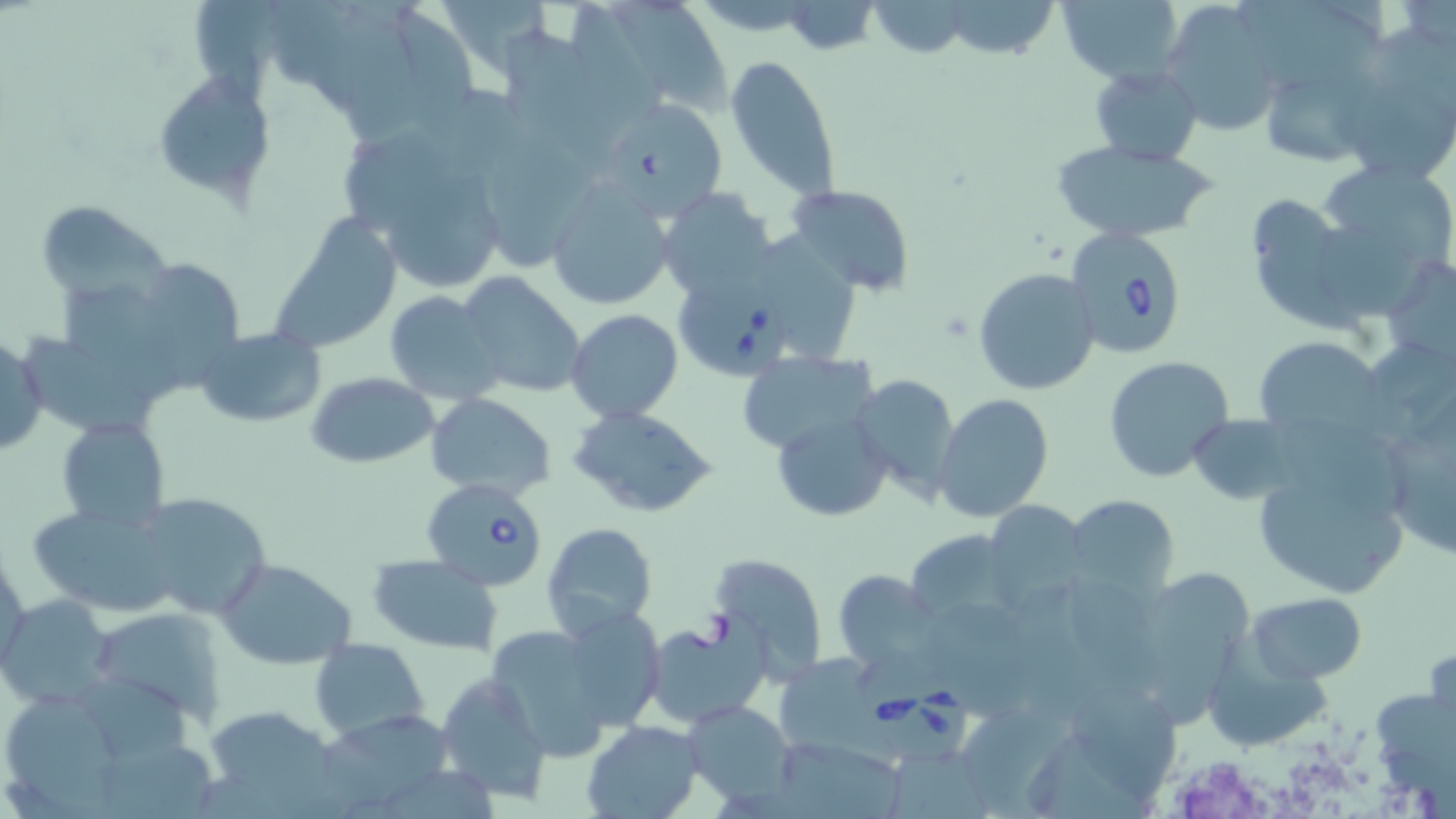
Summary:
  - Coordinate format: approximate bounding boxes as named x1/y1/x2/y2 corners in pixels
  - Uninfected red blood cell locations: (x1=937, y1=0, x2=1063, y2=60), (x1=1055, y1=0, x2=1182, y2=85), (x1=1241, y1=0, x2=1383, y2=78), (x1=193, y1=1, x2=289, y2=114), (x1=615, y1=1, x2=738, y2=112), (x1=868, y1=2, x2=974, y2=58), (x1=1157, y1=2, x2=1285, y2=134), (x1=387, y1=3, x2=476, y2=139), (x1=337, y1=12, x2=420, y2=147), (x1=502, y1=29, x2=623, y2=163), (x1=725, y1=55, x2=841, y2=200), (x1=1089, y1=65, x2=1205, y2=166), (x1=150, y1=70, x2=274, y2=203), (x1=1261, y1=74, x2=1378, y2=168), (x1=1349, y1=80, x2=1456, y2=181), (x1=606, y1=97, x2=730, y2=222), (x1=488, y1=133, x2=601, y2=269), (x1=1051, y1=141, x2=1221, y2=241), (x1=1325, y1=156, x2=1456, y2=271), (x1=392, y1=179, x2=510, y2=291), (x1=544, y1=179, x2=673, y2=313), (x1=786, y1=182, x2=917, y2=297), (x1=656, y1=188, x2=774, y2=302), (x1=1253, y1=198, x2=1366, y2=340), (x1=34, y1=199, x2=169, y2=305), (x1=272, y1=217, x2=401, y2=352), (x1=1311, y1=223, x2=1432, y2=321), (x1=1377, y1=258, x2=1456, y2=369), (x1=147, y1=266, x2=247, y2=387), (x1=973, y1=266, x2=1102, y2=396), (x1=456, y1=271, x2=584, y2=399), (x1=65, y1=284, x2=179, y2=404), (x1=384, y1=290, x2=505, y2=403), (x1=567, y1=309, x2=683, y2=422), (x1=194, y1=327, x2=327, y2=428), (x1=0, y1=332, x2=46, y2=458), (x1=24, y1=338, x2=156, y2=433), (x1=1259, y1=340, x2=1403, y2=440), (x1=736, y1=350, x2=879, y2=456), (x1=1105, y1=356, x2=1235, y2=485), (x1=1375, y1=369, x2=1456, y2=559), (x1=305, y1=371, x2=440, y2=470), (x1=850, y1=372, x2=961, y2=501), (x1=425, y1=393, x2=555, y2=499), (x1=935, y1=394, x2=1053, y2=521), (x1=568, y1=404, x2=717, y2=520), (x1=769, y1=406, x2=892, y2=522), (x1=58, y1=417, x2=169, y2=531), (x1=1276, y1=417, x2=1409, y2=520), (x1=1247, y1=443, x2=1416, y2=600), (x1=131, y1=492, x2=273, y2=621), (x1=1066, y1=495, x2=1179, y2=601), (x1=26, y1=504, x2=180, y2=614), (x1=995, y1=506, x2=1087, y2=617), (x1=540, y1=522, x2=660, y2=642), (x1=914, y1=531, x2=1021, y2=623), (x1=1, y1=542, x2=28, y2=675), (x1=708, y1=551, x2=832, y2=680), (x1=367, y1=554, x2=503, y2=655), (x1=216, y1=558, x2=358, y2=671), (x1=831, y1=569, x2=938, y2=670), (x1=1151, y1=571, x2=1247, y2=735), (x1=1246, y1=592, x2=1367, y2=684), (x1=1, y1=595, x2=117, y2=708), (x1=549, y1=606, x2=668, y2=740), (x1=90, y1=609, x2=228, y2=722), (x1=932, y1=610, x2=1035, y2=721), (x1=645, y1=623, x2=770, y2=729), (x1=485, y1=624, x2=628, y2=762), (x1=309, y1=636, x2=430, y2=744), (x1=774, y1=653, x2=888, y2=755), (x1=434, y1=671, x2=555, y2=805), (x1=84, y1=672, x2=193, y2=760), (x1=1070, y1=681, x2=1186, y2=800), (x1=10, y1=697, x2=122, y2=817), (x1=683, y1=700, x2=796, y2=802), (x1=201, y1=706, x2=338, y2=809), (x1=326, y1=713, x2=457, y2=808), (x1=969, y1=713, x2=1074, y2=818), (x1=581, y1=719, x2=702, y2=819), (x1=776, y1=743, x2=909, y2=819), (x1=100, y1=744, x2=227, y2=819)
  - Babesia divergens-infected red blood cell locations: (x1=1063, y1=225, x2=1187, y2=359), (x1=669, y1=275, x2=791, y2=378), (x1=423, y1=476, x2=549, y2=592), (x1=851, y1=655, x2=973, y2=766)
  - Slide-level diagnosis: Babesia divergens
  - Magnification: 1000x
  - Field of view: one of a larger specimen
  - Preparation: thin blood smear
  - Stain: May-Grünwald-Giemsa
  - Image size: 1456×819 pixels
  - Modality: optical microscopy